Name the blood parasite species.
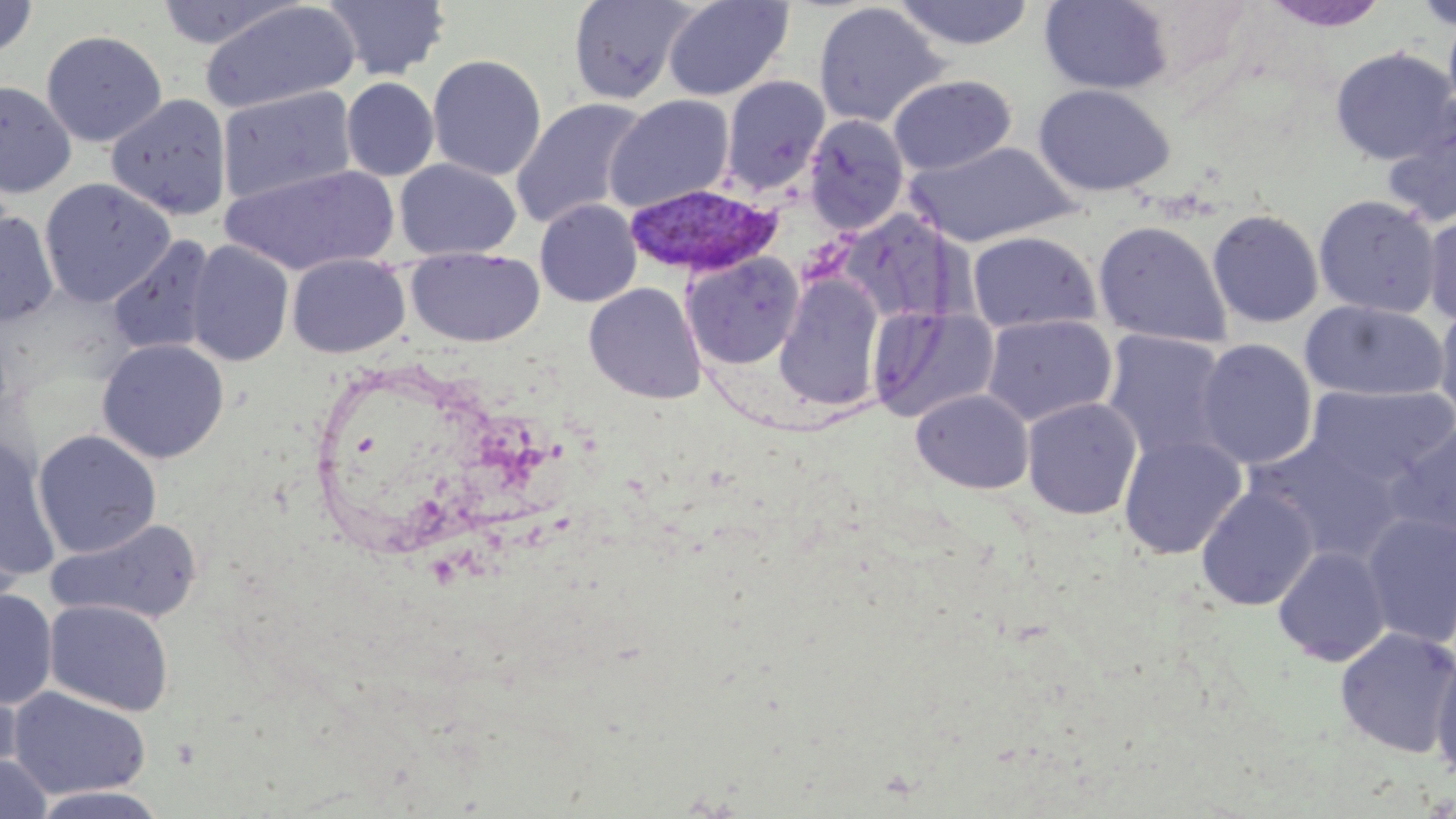

Plasmodium vivax.

Approximate bounding boxes as (x1, y1, x2, y2) in pixels. Uninfected red blood cell locations: (323, 0, 451, 81), (663, 0, 793, 101), (891, 0, 1037, 52), (1039, 0, 1173, 94), (0, 1, 37, 59), (154, 1, 303, 49), (567, 1, 696, 104), (1262, 1, 1391, 33), (1411, 1, 1456, 32), (199, 2, 360, 114), (812, 2, 948, 128), (1442, 7, 1456, 122), (41, 29, 168, 147), (1329, 48, 1455, 165), (427, 54, 547, 181), (888, 74, 1017, 176), (721, 76, 830, 196), (341, 77, 439, 181), (0, 80, 77, 198), (1033, 83, 1176, 197), (217, 86, 357, 206), (106, 93, 232, 220), (605, 94, 735, 213), (510, 97, 649, 231), (1380, 98, 1456, 228), (804, 115, 910, 234), (904, 140, 1080, 247), (394, 158, 521, 260), (221, 163, 399, 276), (38, 178, 177, 307), (1313, 194, 1441, 318), (534, 199, 642, 307), (1207, 208, 1324, 328), (1423, 208, 1456, 327), (0, 210, 59, 326), (1093, 220, 1232, 347), (966, 230, 1101, 333), (106, 235, 217, 356), (185, 241, 295, 367), (406, 248, 545, 348), (682, 252, 804, 369), (287, 253, 410, 358), (774, 274, 885, 412), (584, 282, 706, 404), (1300, 300, 1450, 403), (1434, 304, 1456, 423), (867, 306, 999, 423), (981, 314, 1118, 427), (1101, 330, 1233, 466), (96, 338, 230, 464), (1194, 338, 1318, 470), (1304, 384, 1456, 487), (911, 388, 1034, 494), (1021, 397, 1142, 520), (1385, 423, 1456, 552), (33, 429, 162, 558), (1119, 434, 1246, 560), (1249, 434, 1407, 563), (0, 437, 61, 581), (1196, 485, 1319, 610), (1361, 512, 1456, 648), (46, 518, 203, 625), (0, 519, 27, 623), (1273, 545, 1392, 666), (0, 589, 57, 708), (45, 599, 174, 716), (1334, 626, 1456, 758), (1430, 648, 1456, 784), (0, 673, 24, 785), (8, 686, 152, 799), (0, 753, 52, 819), (29, 786, 170, 819). Plasmodium vivax-infected red blood cell locations: (623, 183, 782, 278). May-Grünwald-Giemsa-stained preparation. Image is 1456×819 pixels. Light microscopy. 1000x magnification. One field of a larger specimen. Thin blood smear.